Name the blood parasite species.
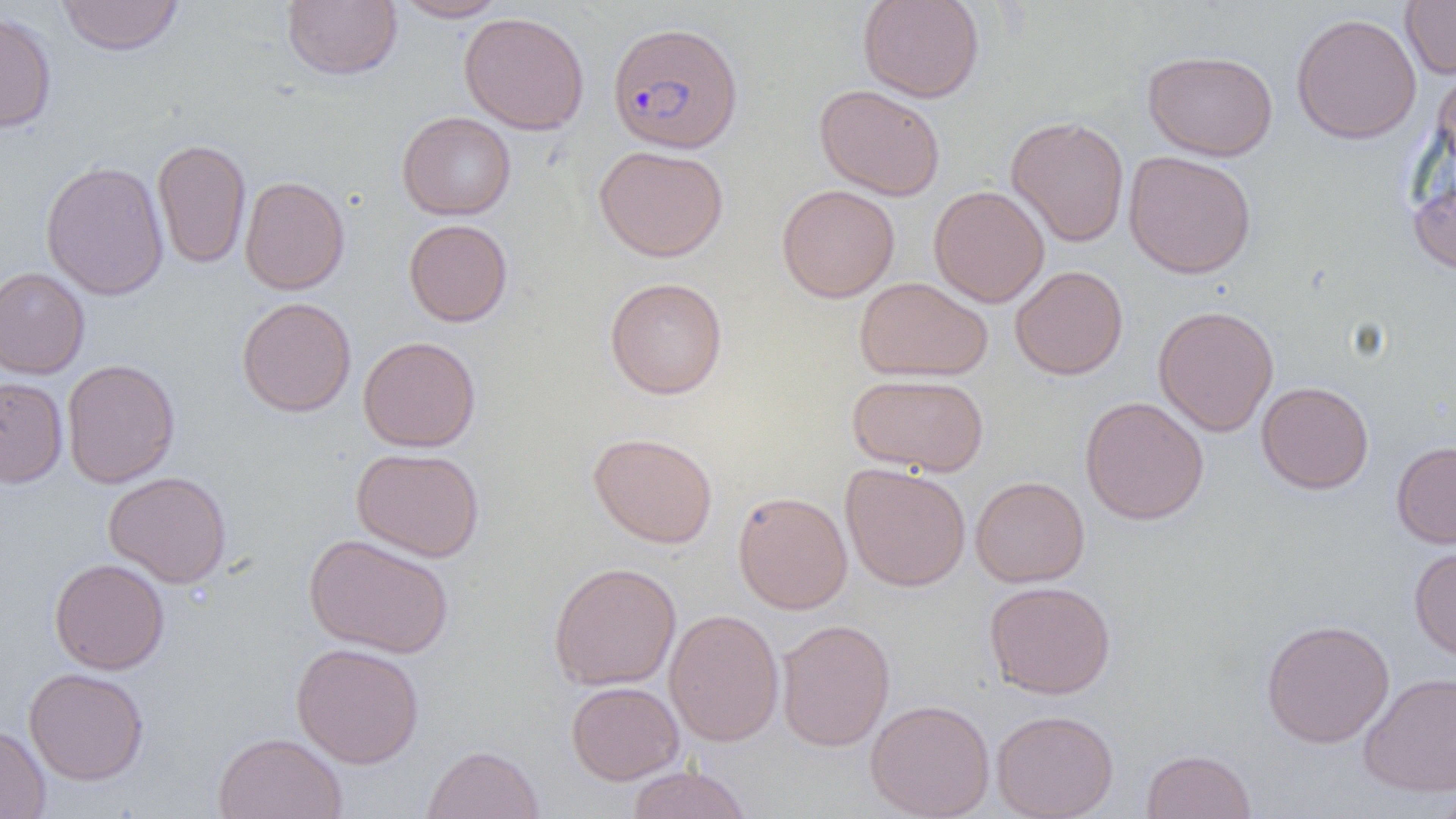

Plasmodium falciparum.

{
  "uninfected_red_blood_cell_locations": "approximate bounding boxes as (x1,y1)-(x2,y2) corner pairs in pixels: (56,0)-(184,56), (282,0)-(402,81), (391,0)-(510,22), (857,0)-(985,103), (1400,0)-(1456,79), (0,10)-(57,134), (459,12)-(590,135), (1291,12)-(1422,145), (1142,49)-(1278,161), (1432,64)-(1456,178), (814,84)-(945,201), (397,111)-(517,220), (1005,116)-(1130,247), (152,138)-(251,269), (594,144)-(729,262), (1124,150)-(1257,279), (40,160)-(170,300), (1407,162)-(1456,277), (240,175)-(350,295), (777,184)-(900,303), (928,185)-(1050,307), (403,219)-(513,327), (1010,265)-(1128,380), (0,267)-(90,379), (854,276)-(993,382), (604,277)-(728,399), (236,297)-(357,417), (1153,305)-(1279,437), (358,335)-(481,452), (62,359)-(180,488), (847,373)-(989,475), (0,377)-(68,488), (1256,381)-(1374,494), (1080,396)-(1209,526), (588,431)-(719,548), (1391,440)-(1456,549), (350,447)-(484,561), (841,463)-(971,592), (103,471)-(232,588), (970,475)-(1090,587), (732,490)-(853,614), (303,533)-(455,658), (1409,543)-(1456,662), (49,557)-(169,675), (548,561)-(681,691), (984,580)-(1116,699), (664,608)-(784,747), (1261,618)-(1395,748), (776,619)-(895,752), (290,642)-(425,768), (23,667)-(149,786), (1359,672)-(1456,796), (566,680)-(684,785), (865,698)-(995,819), (991,709)-(1119,819), (0,723)-(50,819), (213,732)-(347,819), (421,744)-(544,819), (1141,749)-(1257,819), (625,764)-(753,819), (1432,786)-(1456,819)",
  "preparation": "thin blood film",
  "image_size": "1456×819 pixels",
  "modality": "light microscopy",
  "field_of_view": "one of a larger specimen",
  "plasmodium_falciparum_infected_red_blood_cell_locations": "approximate bounding boxes as (x1,y1)-(x2,y2) corner pairs in pixels: (607,21)-(744,154)",
  "magnification": "1000x"
}